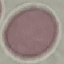

{
  "malaria_status": "uninfected",
  "stain": "Giemsa",
  "image_type": "cell patch, automatically extracted from a larger field of view and resized to 64 × 64 pixels",
  "capture": "smartphone through the microscope eyepiece",
  "preparation": "thin blood film"
}